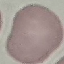

result = no malaria parasites detected
capture = smartphone through the microscope eyepiece
stain = Giemsa
preparation = thin smear
image type = cell patch, automatically extracted from a larger field of view and resized to 64 × 64 pixels